Assess the morphology of the erythrocytes.
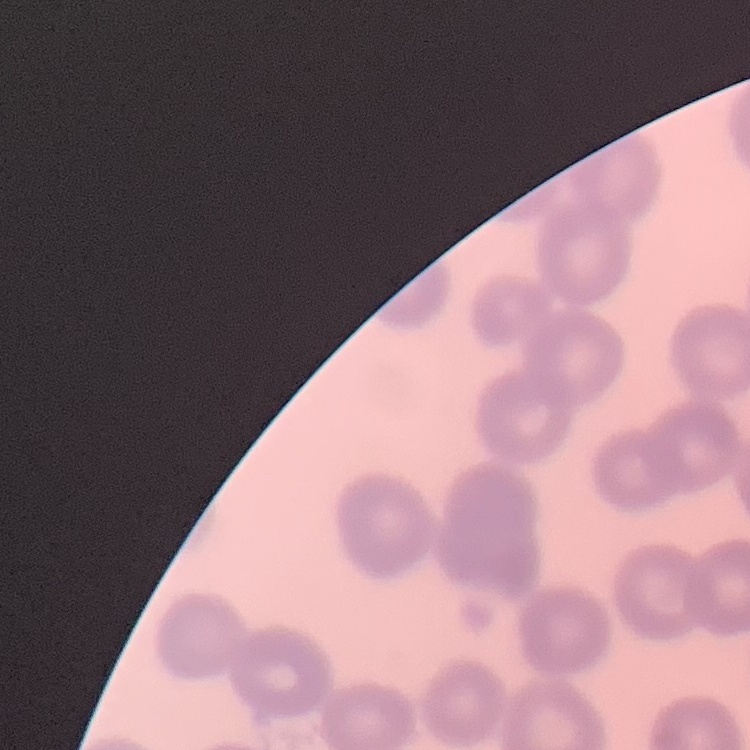
No rouleaux formation.

Summary:
  - Stain: Field's or Giemsa
  - Image type: one tile cut from a larger photomicrograph
  - Preparation: thin blood film